State which parasite is depicted.
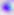
This is Toxoplasma gondii.

modality = micrograph
magnification = 400x